Report the malaria status of this cell.
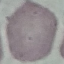
Uninfected.

Summary:
  - Capture: smartphone camera at the microscope eyepiece
  - Image type: cell patch, automatically extracted from a larger field of view and resized to 64 × 64 pixels
  - Preparation: thin blood smear
  - Stain: Giemsa